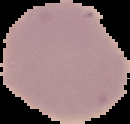
From a thin blood film. Image is 130×124 pixels. Result: negative for Plasmodium parasites. Segmented cell region on a black background.